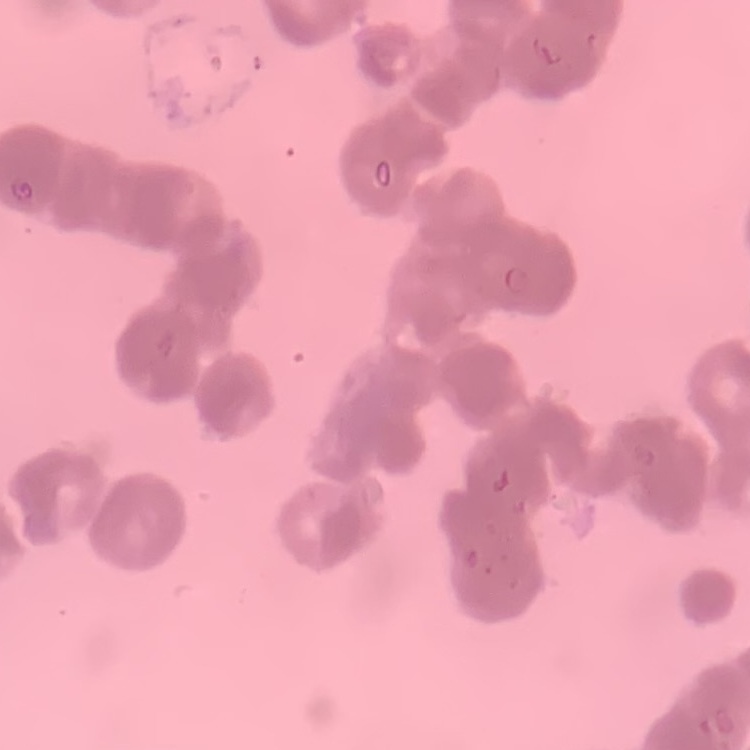

Summary:
  - Erythrocyte morphology: rouleaux formation
  - Preparation: thin peripheral smear
  - Image type: square crop of a larger photomicrograph
  - Stain: Field's or Giemsa